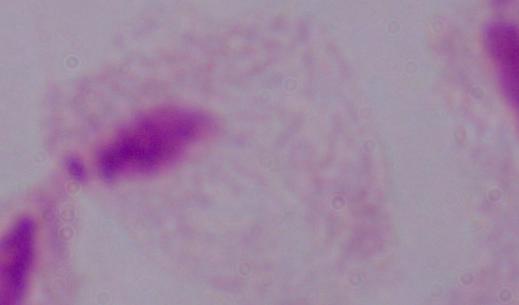
Summary:
  - Magnification: 1000x
  - Identification: trichomonad
  - Modality: photomicrograph